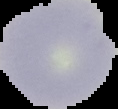
result = Plasmodium parasites detected
image type = segmented cell region with the area outside set to black
preparation = thin blood film
image size = 118×109 pixels